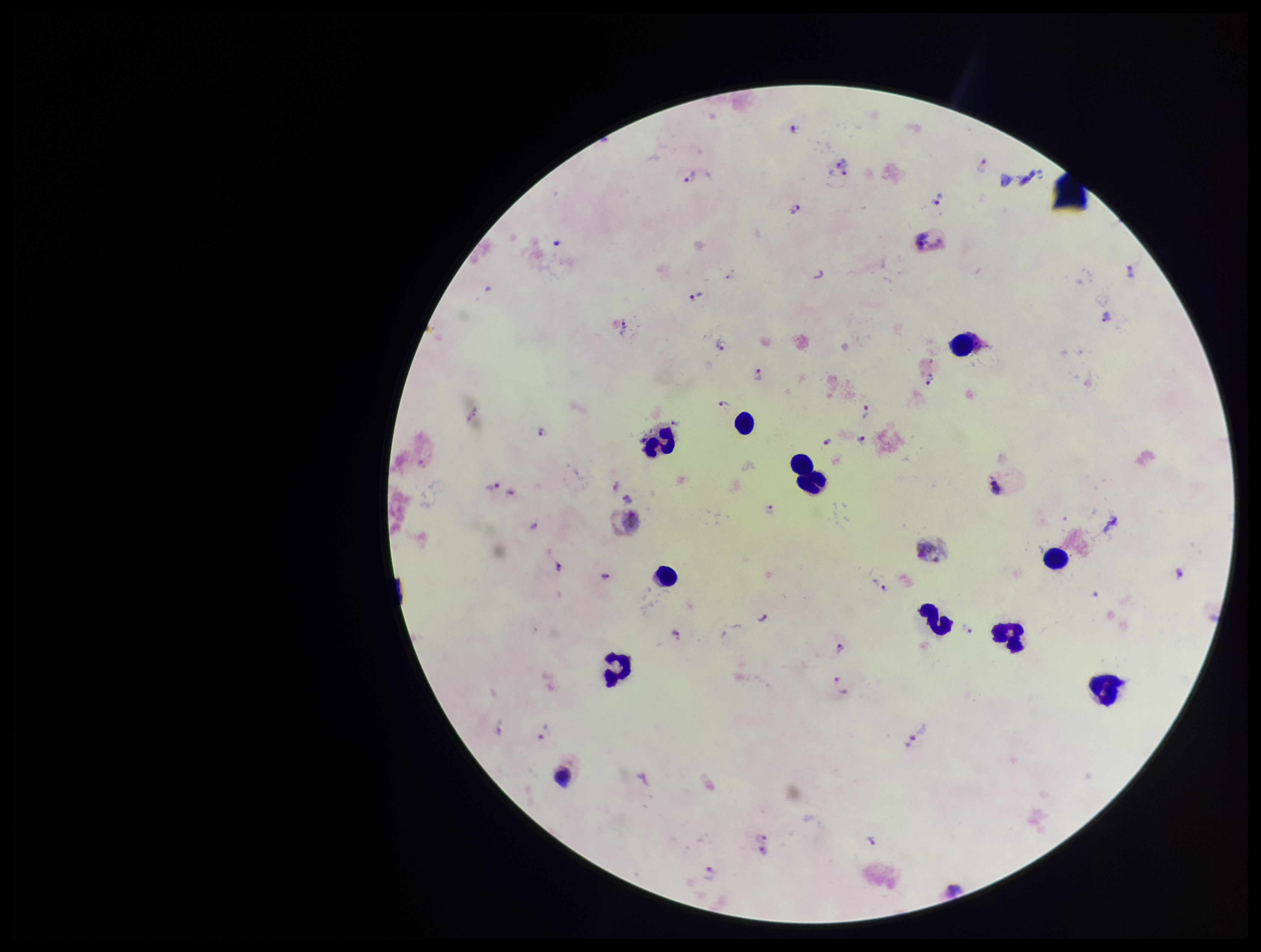
image size = 1261×952 pixels
preparation = thick blood smear
capture = smartphone photograph through the microscope eyepiece
Plasmodium parasites = identified
patient malaria status = positive
species reported for this patient = Plasmodium vivax
field of view = single
leukocyte count = 11
parasite count = 29
stain = Giemsa